Assess this cell for malaria.
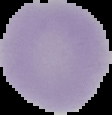
It is uninfected.

{
  "image_size": "112×115 pixels",
  "image_type": "segmented cell region on a black background",
  "preparation": "thin blood film"
}